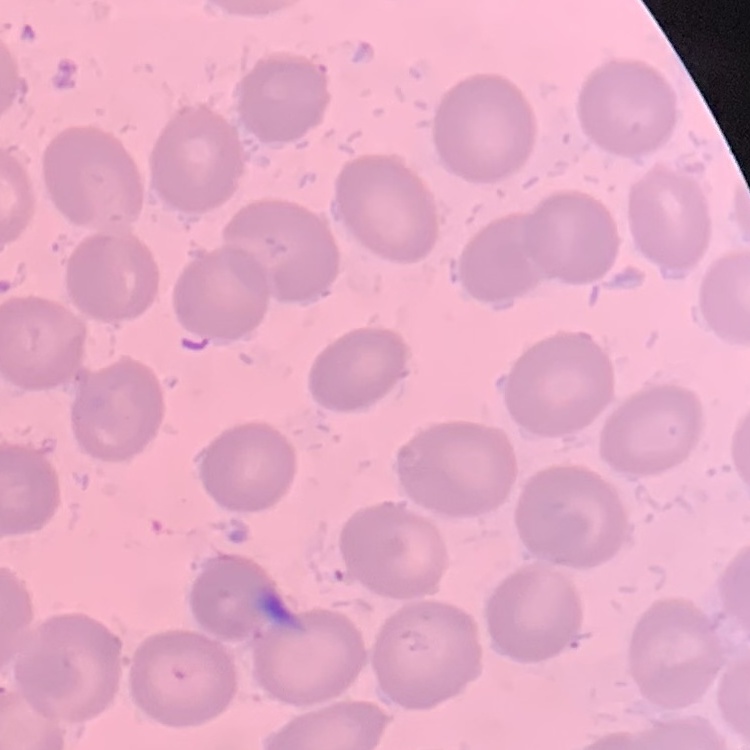
Summary:
  - Erythrocyte morphology: no rouleaux formation
  - Preparation: thin blood smear
  - Stain: Field's or Giemsa
  - Image type: one tile cut from a larger photomicrograph